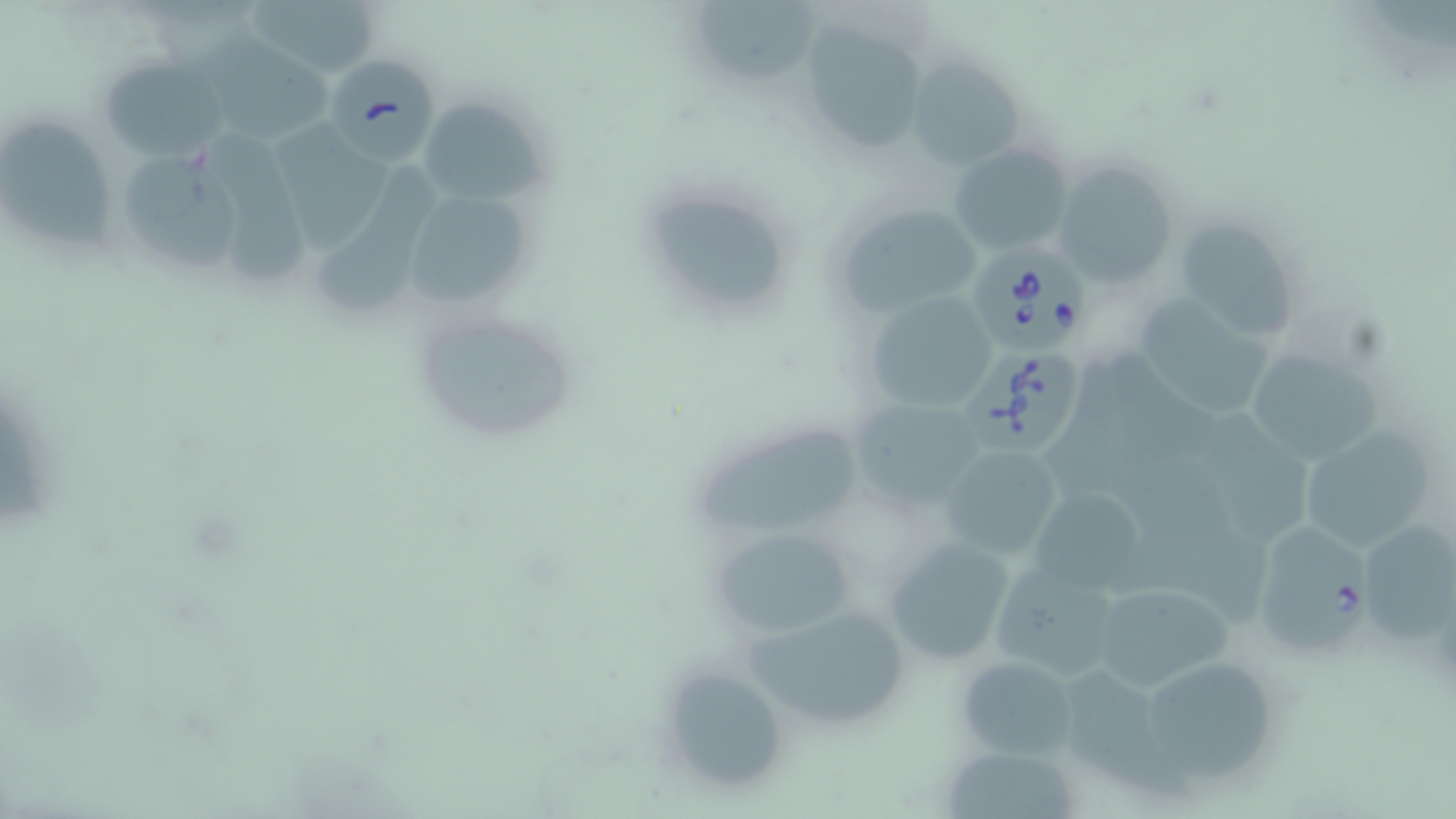

Approximate bounding boxes as [x1, y1, x2, y2] in pixels. Uninfected red blood cell locations: [242, 0, 385, 80], [692, 0, 814, 80], [800, 21, 932, 159], [205, 36, 334, 139], [903, 53, 1030, 173], [101, 55, 229, 159], [415, 96, 551, 204], [273, 123, 394, 249], [3, 124, 117, 255], [213, 133, 318, 287], [947, 142, 1072, 256], [125, 157, 240, 272], [1053, 161, 1180, 288], [314, 169, 437, 314], [406, 196, 539, 308], [642, 198, 792, 310], [830, 199, 984, 320], [1170, 220, 1298, 332], [866, 292, 997, 415], [1144, 295, 1275, 420], [408, 303, 583, 450], [1244, 354, 1386, 461], [855, 402, 983, 503], [1196, 413, 1317, 546], [1292, 418, 1443, 560], [694, 428, 858, 538], [940, 445, 1064, 562], [1023, 481, 1151, 599], [712, 526, 856, 637], [880, 536, 1016, 667], [987, 557, 1128, 682], [1088, 579, 1234, 694], [741, 601, 915, 735], [954, 656, 1078, 759], [653, 661, 792, 797], [1054, 663, 1188, 803], [1148, 665, 1279, 787], [948, 749, 1085, 819]. Babesia divergens-infected red blood cell locations: [327, 53, 441, 166], [972, 239, 1095, 356], [962, 344, 1085, 457], [1257, 519, 1378, 653]. Slide-level diagnosis: Babesia divergens. May-Grünwald-Giemsa stain. Optical microscopy. 1000x magnification. Thin blood smear. Image is 1456×819 pixels. One field of a larger specimen.